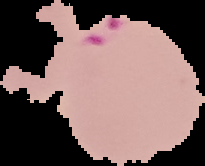

Summary:
  - Preparation: thin blood film
  - Image size: 205×166 pixels
  - Image type: segmented cell region with the area outside set to black
  - Malaria status: parasitized